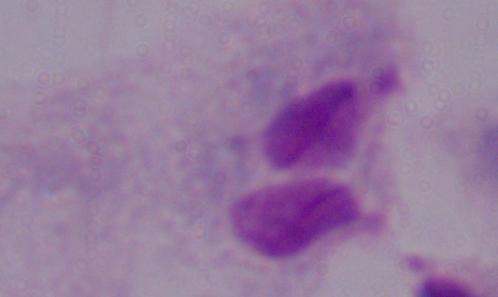
modality = photomicrograph
magnification = 1000x
identification = trichomonad